Report the malaria status of this cell.
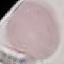
Uninfected.

{
  "capture": "smartphone camera at the microscope eyepiece",
  "preparation": "thin blood smear",
  "stain": "Giemsa",
  "image_type": "automatically extracted cell patch, resized to 64 × 64 pixels"
}